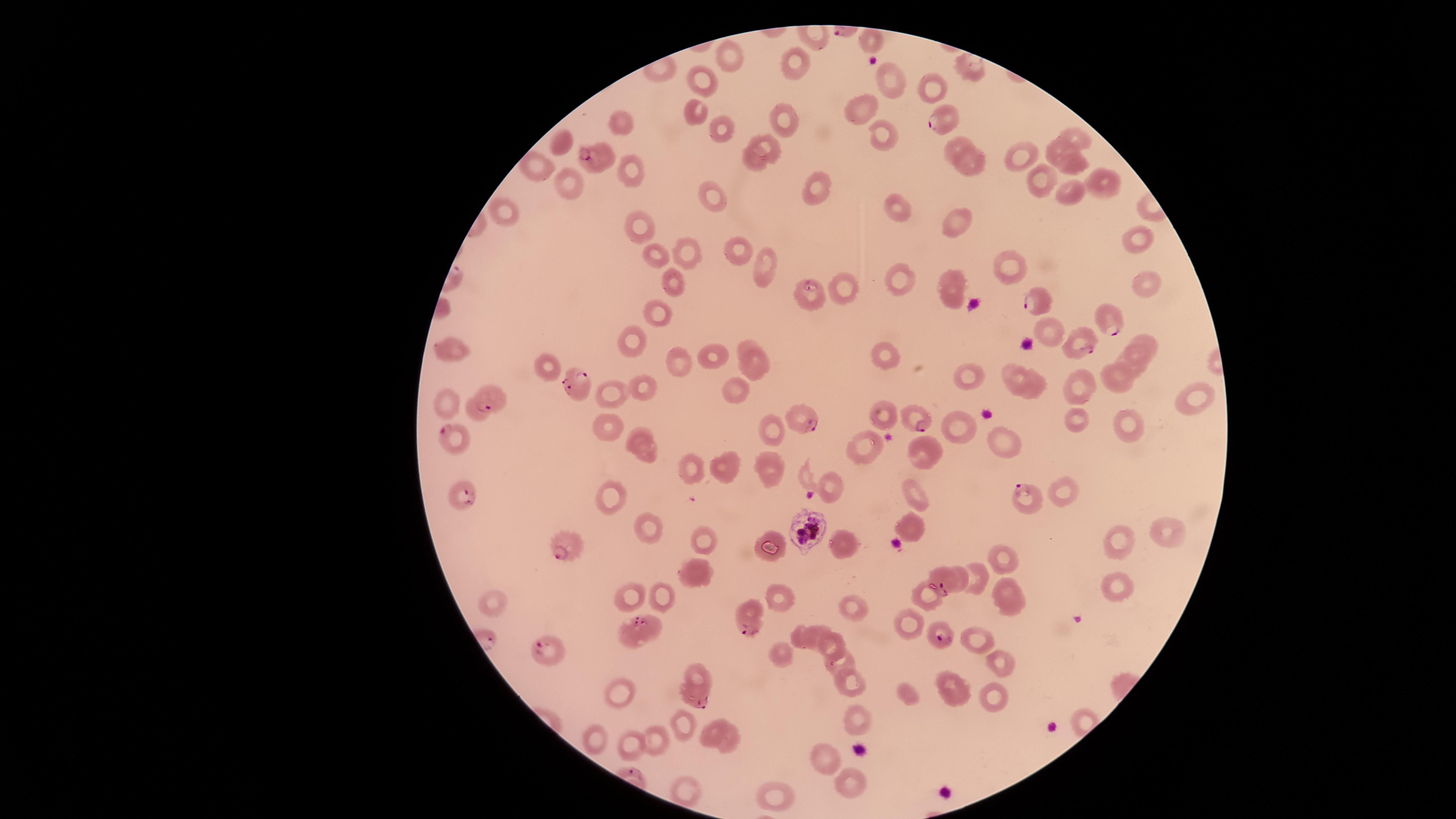

Approximate marker points as (x, y) in pixels.
Summary:
  - Uninfected red blood cells: (871, 41), (726, 52), (795, 62), (705, 80), (889, 81), (927, 85), (863, 109), (696, 110), (621, 118), (782, 118), (717, 130), (882, 132), (1075, 134), (564, 137), (764, 140), (955, 145), (1055, 150), (1022, 154), (755, 159), (968, 162), (1073, 164), (532, 168), (636, 168), (568, 176), (1039, 179), (817, 186), (1104, 186), (710, 191), (1066, 192), (505, 209), (898, 209), (639, 223), (962, 228), (1134, 239), (738, 244), (687, 247), (648, 254), (765, 264), (1010, 265), (898, 275), (951, 276), (676, 280), (1145, 286), (841, 287), (952, 294), (661, 314), (1149, 341), (744, 342), (627, 343), (452, 348), (887, 352), (715, 356), (677, 358), (1134, 359), (752, 364), (544, 366), (971, 372), (1014, 377), (1116, 378), (640, 386), (1033, 386), (1082, 386), (732, 389), (612, 393), (1197, 399), (444, 401), (882, 411), (475, 413), (1073, 417), (772, 422), (1129, 422), (957, 426), (607, 427), (637, 434), (1006, 434), (866, 447), (927, 451), (649, 452), (768, 461), (724, 462), (691, 465), (834, 481), (1066, 488), (610, 495), (919, 496), (910, 522), (649, 525), (1166, 531), (702, 535), (1121, 539), (844, 542), (769, 544), (1003, 555), (698, 572), (977, 573), (961, 584), (1004, 584), (1115, 587), (780, 595), (633, 596), (664, 597), (927, 598), (497, 599), (1015, 606), (849, 607), (651, 620), (908, 625), (801, 629), (822, 630), (978, 639), (836, 645), (782, 656), (997, 661), (843, 663), (695, 677), (855, 682), (954, 689), (619, 693), (908, 694), (997, 699), (856, 713), (681, 716), (714, 729), (660, 735), (598, 739), (728, 741), (627, 746), (823, 756), (851, 781), (689, 788), (780, 795)
  - Parasitized red blood cells: (942, 119), (591, 159), (809, 293), (1040, 307), (1111, 321), (1081, 346), (577, 383), (492, 396), (800, 415), (917, 419), (454, 436), (464, 494), (1025, 497), (805, 526), (565, 545), (944, 580), (749, 615), (631, 631), (941, 634), (550, 652), (695, 703)
  - Visible region: circular
  - Capture: smartphone photograph through the microscope eyepiece
  - Stain: Giemsa
  - Image size: 1456×819 pixels
  - Presence: malaria parasites identified
  - Preparation: thin blood smear
  - Field of view: single
  - Species: Plasmodium falciparum